Classify this cell by malaria status.
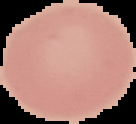

Uninfected.

image size = 136×124 pixels
preparation = thin blood film
image type = segmented cell region with the area outside set to black